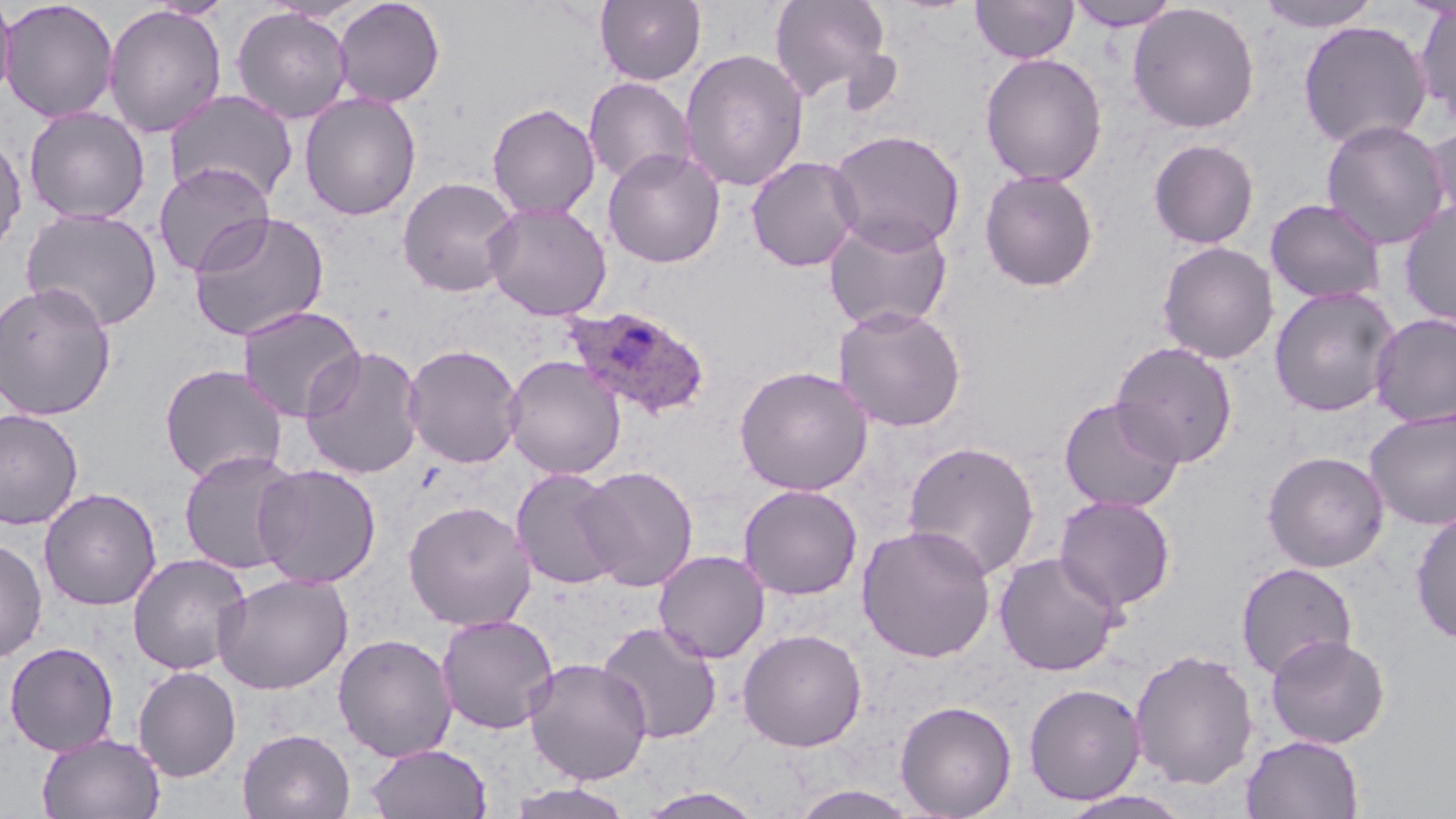
slide-level diagnosis = Plasmodium ovale
magnification = 1000x
Plasmodium ovale-infected red blood cell locations = approximate bounding boxes as (x1,y1)-(x2,y2) corner pairs in pixels: (562,304)-(712,421)
stain = May-Grünwald-Giemsa
preparation = thin blood smear
uninfected red blood cell locations = approximate bounding boxes as (x1,y1)-(x2,y2) corner pairs in pixels: (0,0)-(119,123), (0,0)-(17,110), (333,0)-(445,107), (595,0)-(706,86), (768,0)-(894,103), (971,0)-(1078,63), (1065,0)-(1182,31), (1255,0)-(1383,32), (1127,2)-(1260,134), (1413,3)-(1456,129), (102,4)-(227,139), (230,6)-(354,124), (1297,19)-(1432,150), (679,48)-(809,192), (980,53)-(1107,186), (583,77)-(695,187), (164,89)-(298,205), (299,92)-(421,221), (487,102)-(600,219), (24,106)-(151,225), (1320,119)-(1451,250), (1424,122)-(1456,232), (828,129)-(965,253), (0,130)-(27,259), (1148,138)-(1260,250), (603,147)-(725,268), (746,155)-(864,272), (153,163)-(274,277), (979,168)-(1099,292), (397,176)-(521,297), (1265,198)-(1386,305), (1397,200)-(1456,326), (482,201)-(612,321), (20,207)-(164,333), (188,211)-(330,342), (822,212)-(954,333), (1157,241)-(1278,364), (0,282)-(117,420), (1269,286)-(1401,417), (237,305)-(366,422), (833,305)-(967,432), (1370,313)-(1456,428), (1111,341)-(1239,468), (403,344)-(524,469), (299,345)-(425,480), (503,355)-(626,480), (158,364)-(288,484), (734,365)-(873,496), (1059,396)-(1185,513), (0,408)-(84,530), (1364,409)-(1456,529), (901,440)-(1040,580), (178,448)-(303,575), (1262,451)-(1389,572), (253,463)-(381,588), (576,465)-(699,591), (510,468)-(626,590), (738,484)-(863,600), (39,487)-(161,611), (1054,495)-(1176,612), (402,500)-(537,631), (1410,508)-(1456,644), (856,524)-(996,662), (0,536)-(47,664), (653,549)-(770,663), (994,551)-(1125,676), (127,553)-(252,675), (1235,562)-(1358,679), (214,572)-(353,695), (436,614)-(559,734), (596,621)-(723,744), (737,627)-(868,752), (333,633)-(457,762), (1265,634)-(1391,749), (3,641)-(119,756), (1129,648)-(1259,790), (523,658)-(653,784), (133,665)-(242,782), (1023,682)-(1146,805), (895,700)-(1017,818), (238,728)-(355,819), (36,733)-(166,818), (1241,735)-(1365,818), (364,743)-(492,819), (504,782)-(637,819), (790,784)-(923,819), (636,786)-(768,818), (1056,789)-(1196,819)
modality = optical microscopy
field of view = single
image size = 1456×819 pixels